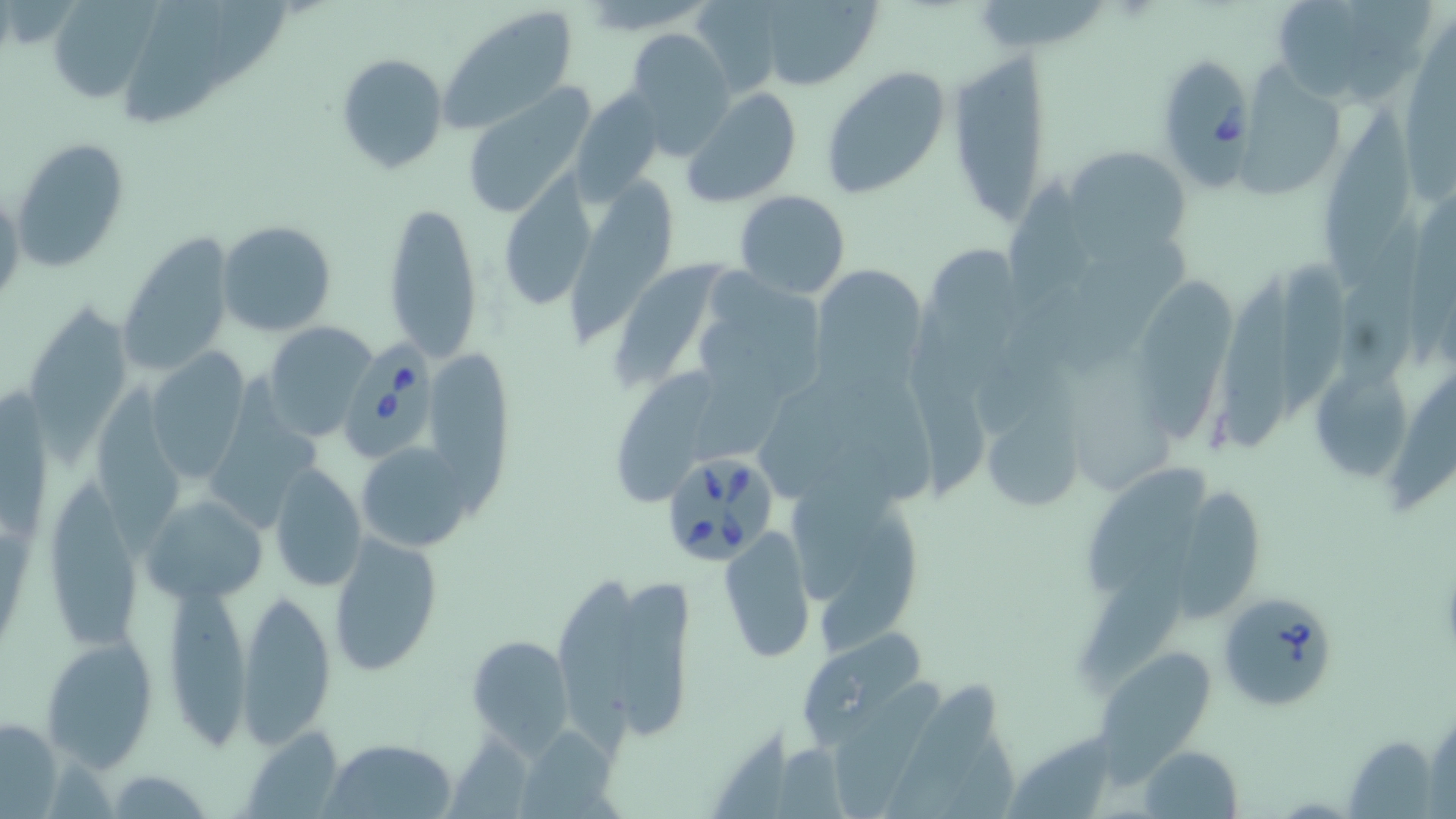

Babesia divergens-infected red blood cell locations = approximate bounding boxes as named x1/y1/x2/y2 corners in pixels: (x1=1164, y1=54, x2=1257, y2=197), (x1=343, y1=331, x2=441, y2=461), (x1=659, y1=449, x2=781, y2=568), (x1=1220, y1=588, x2=1340, y2=711)
slide-level diagnosis = Babesia divergens
image size = 1456×819 pixels
stain = May-Grünwald-Giemsa
uninfected red blood cell locations = approximate bounding boxes as named x1/y1/x2/y2 corners in pixels: (x1=688, y1=0, x2=788, y2=97), (x1=752, y1=0, x2=883, y2=90), (x1=1269, y1=0, x2=1432, y2=107), (x1=46, y1=1, x2=155, y2=103), (x1=438, y1=5, x2=581, y2=134), (x1=624, y1=28, x2=736, y2=154), (x1=946, y1=51, x2=1052, y2=227), (x1=334, y1=53, x2=449, y2=175), (x1=1244, y1=63, x2=1347, y2=203), (x1=818, y1=65, x2=949, y2=199), (x1=463, y1=85, x2=597, y2=220), (x1=568, y1=85, x2=668, y2=203), (x1=683, y1=88, x2=803, y2=208), (x1=1320, y1=103, x2=1414, y2=291), (x1=10, y1=137, x2=130, y2=272), (x1=1064, y1=144, x2=1191, y2=252), (x1=503, y1=172, x2=599, y2=302), (x1=568, y1=174, x2=675, y2=339), (x1=1006, y1=183, x2=1106, y2=315), (x1=0, y1=189, x2=25, y2=311), (x1=733, y1=189, x2=851, y2=299), (x1=383, y1=199, x2=484, y2=364), (x1=217, y1=219, x2=337, y2=337), (x1=117, y1=230, x2=236, y2=376), (x1=1080, y1=243, x2=1196, y2=366), (x1=1284, y1=252, x2=1346, y2=421), (x1=612, y1=256, x2=724, y2=384), (x1=1218, y1=262, x2=1303, y2=453), (x1=811, y1=264, x2=926, y2=391), (x1=1138, y1=274, x2=1236, y2=444), (x1=691, y1=282, x2=825, y2=412), (x1=25, y1=303, x2=134, y2=443), (x1=906, y1=312, x2=995, y2=494), (x1=262, y1=321, x2=379, y2=441), (x1=434, y1=350, x2=522, y2=531), (x1=146, y1=351, x2=250, y2=481), (x1=1321, y1=353, x2=1407, y2=484), (x1=1398, y1=370, x2=1456, y2=505), (x1=614, y1=373, x2=719, y2=509), (x1=213, y1=375, x2=323, y2=526), (x1=94, y1=383, x2=190, y2=553), (x1=976, y1=406, x2=1085, y2=514), (x1=355, y1=440, x2=476, y2=553), (x1=1087, y1=454, x2=1209, y2=595), (x1=268, y1=465, x2=367, y2=592), (x1=782, y1=476, x2=926, y2=640), (x1=1181, y1=481, x2=1263, y2=622), (x1=47, y1=484, x2=143, y2=645), (x1=145, y1=494, x2=264, y2=601), (x1=1093, y1=522, x2=1215, y2=689), (x1=719, y1=526, x2=817, y2=663), (x1=328, y1=531, x2=445, y2=677), (x1=557, y1=574, x2=697, y2=744), (x1=162, y1=586, x2=255, y2=753), (x1=236, y1=589, x2=337, y2=746), (x1=799, y1=630, x2=929, y2=746), (x1=467, y1=632, x2=573, y2=753), (x1=42, y1=635, x2=159, y2=770), (x1=1100, y1=654, x2=1210, y2=791), (x1=885, y1=680, x2=1007, y2=819), (x1=828, y1=681, x2=945, y2=817), (x1=0, y1=716, x2=63, y2=814), (x1=531, y1=724, x2=628, y2=819), (x1=242, y1=727, x2=346, y2=818), (x1=1344, y1=736, x2=1435, y2=819), (x1=322, y1=737, x2=456, y2=818), (x1=1136, y1=745, x2=1242, y2=818), (x1=104, y1=767, x2=215, y2=818)
preparation = thin blood film
magnification = 1000x
modality = light microscopy
field of view = one of a larger specimen